State which cell type is depicted.
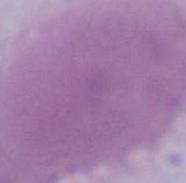
An erythrocyte.

Captured at 1000x magnification. Photomicrograph.